Locate and identify every blood parasite.
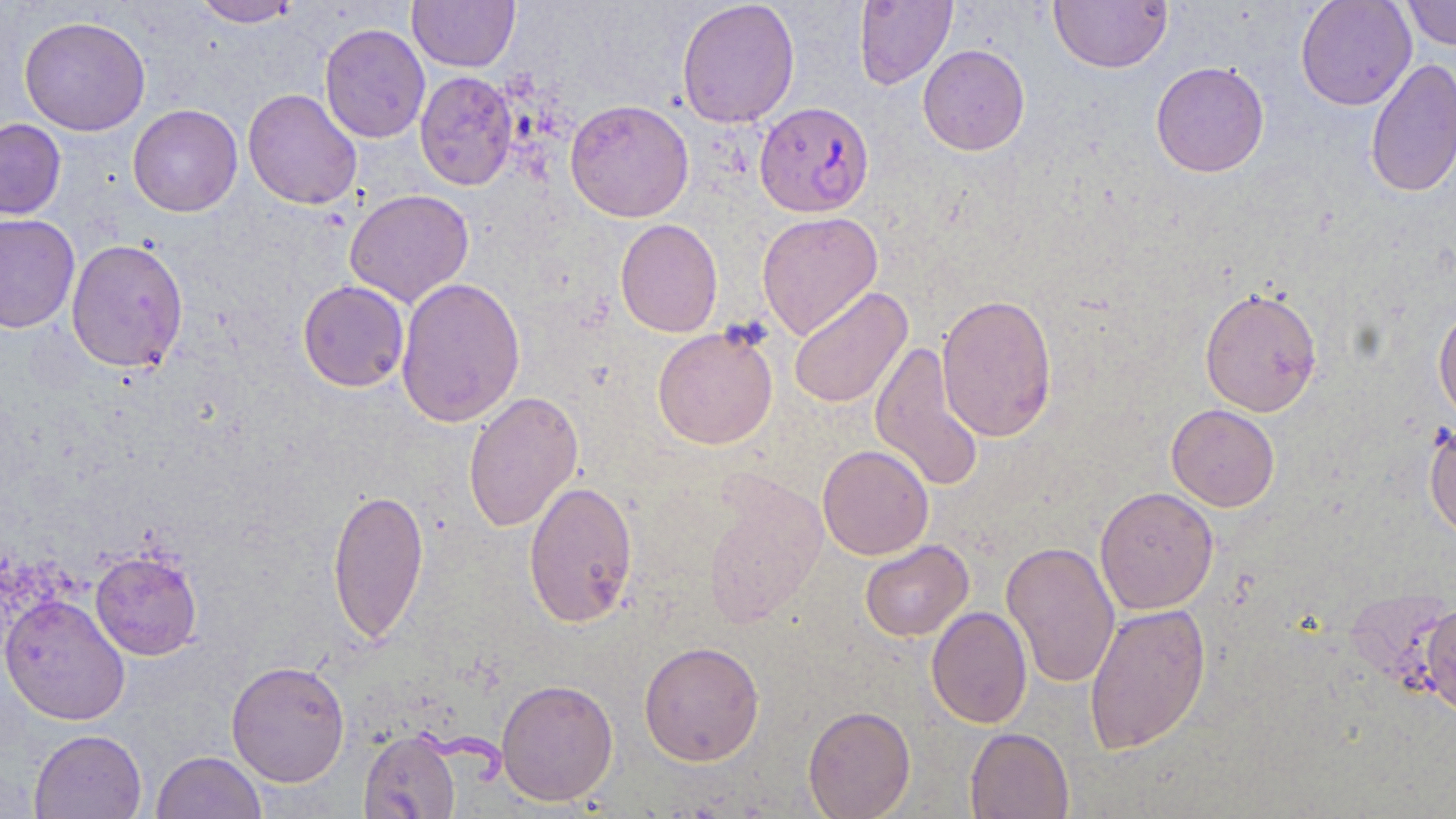
Approximate bounding boxes as [x1, y1, x2, y2] in pixels.
Plasmodium falciparum-infected red blood cells: [754, 101, 874, 217].
No Plasmodium ovale, Plasmodium malariae, Plasmodium vivax, Babesia divergens, or Trypanosoma brucei observed.

Uninfected red blood cell locations: [192, 0, 301, 27], [407, 0, 520, 72], [676, 0, 800, 128], [853, 0, 957, 89], [1048, 0, 1172, 73], [1295, 0, 1417, 111], [1402, 0, 1456, 50], [18, 15, 151, 136], [319, 23, 430, 143], [918, 44, 1030, 156], [1365, 58, 1456, 198], [1150, 61, 1269, 177], [415, 71, 519, 190], [242, 88, 362, 210], [565, 99, 694, 222], [128, 104, 243, 217], [0, 118, 66, 220], [344, 189, 474, 307], [757, 211, 883, 340], [0, 214, 80, 333], [615, 218, 722, 337], [66, 237, 188, 372], [395, 276, 526, 428], [298, 280, 410, 392], [788, 286, 912, 409], [1199, 286, 1323, 417], [935, 293, 1058, 443], [1433, 302, 1456, 424], [652, 326, 778, 450], [870, 340, 984, 494], [463, 390, 583, 532], [1166, 404, 1280, 511], [1423, 419, 1456, 542], [817, 444, 934, 560], [702, 473, 828, 626], [523, 479, 638, 629], [327, 486, 429, 644], [1095, 486, 1219, 615], [860, 540, 974, 641], [1001, 540, 1120, 689], [90, 549, 203, 660], [1, 594, 130, 725], [1420, 601, 1456, 719], [1084, 602, 1211, 755], [926, 606, 1032, 729], [639, 641, 765, 766], [226, 660, 350, 787], [496, 678, 619, 806], [803, 705, 916, 818], [29, 728, 147, 818], [965, 728, 1074, 818], [359, 729, 460, 819], [151, 751, 267, 819]. Slide-level diagnosis: Plasmodium falciparum. One field of a larger specimen. Image is 1456×819 pixels. Light microscopy. May-Grünwald-Giemsa stain. Captured at 1000x magnification. Thin blood film.